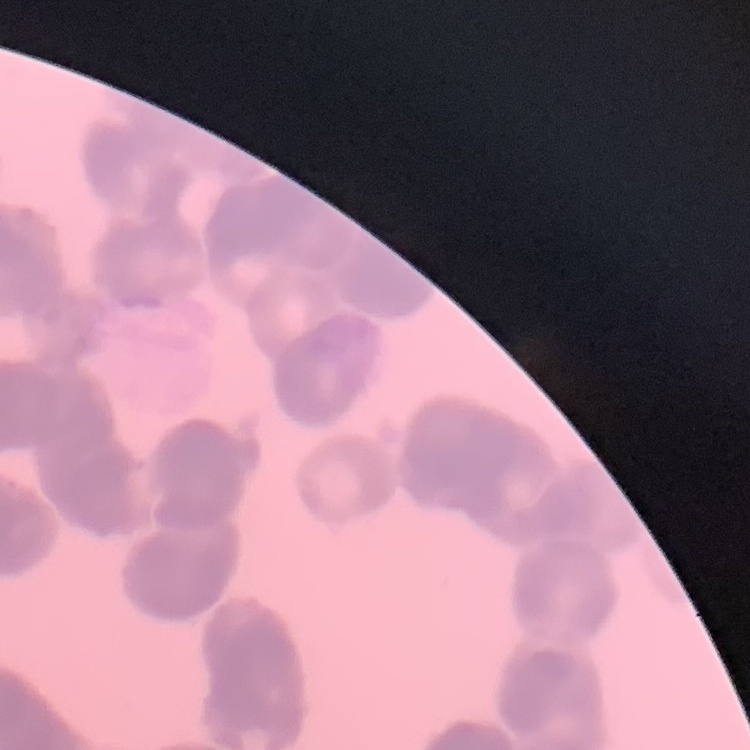

Summary:
  - Red blood cell morphology: rouleaux formation
  - Stain: Field's or Giemsa
  - Image type: one tile cut from a larger photomicrograph
  - Preparation: thin blood film